State which parasite is depicted.
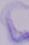
This is a trypanosome.

magnification = 1000x
modality = photomicrograph